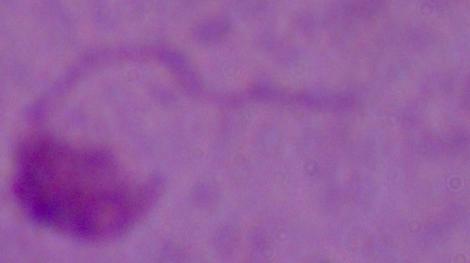
A Leishmania parasite is seen. Micrograph. Captured at 1000x magnification.